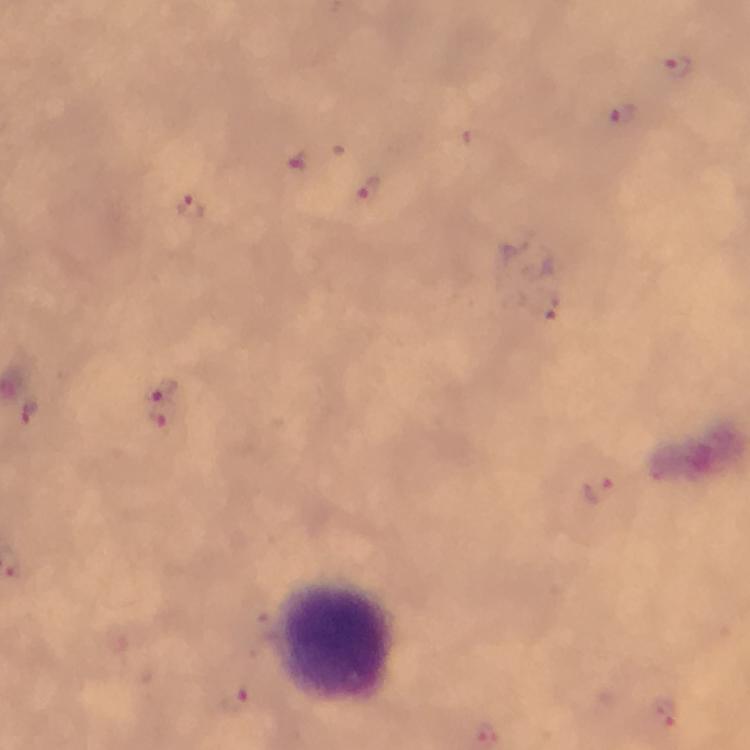

{
  "stain": "Giemsa",
  "leukocyte_locations": "approximate centers as (x, y) in pixels: (335, 642)",
  "capture": "smartphone camera through the microscope",
  "plasmodium_parasite_locations": "approximate centers as (x, y) in pixels: (675, 65), (623, 119), (296, 162), (367, 190), (192, 209), (161, 388), (29, 412), (167, 419), (595, 489), (668, 717)",
  "context": "from a diagnostic examination for malaria",
  "immersion_oil": "used",
  "preparation": "thick blood film",
  "cropped_from": "one field of view",
  "magnification": "100x",
  "image_size": "750×750 pixels"
}